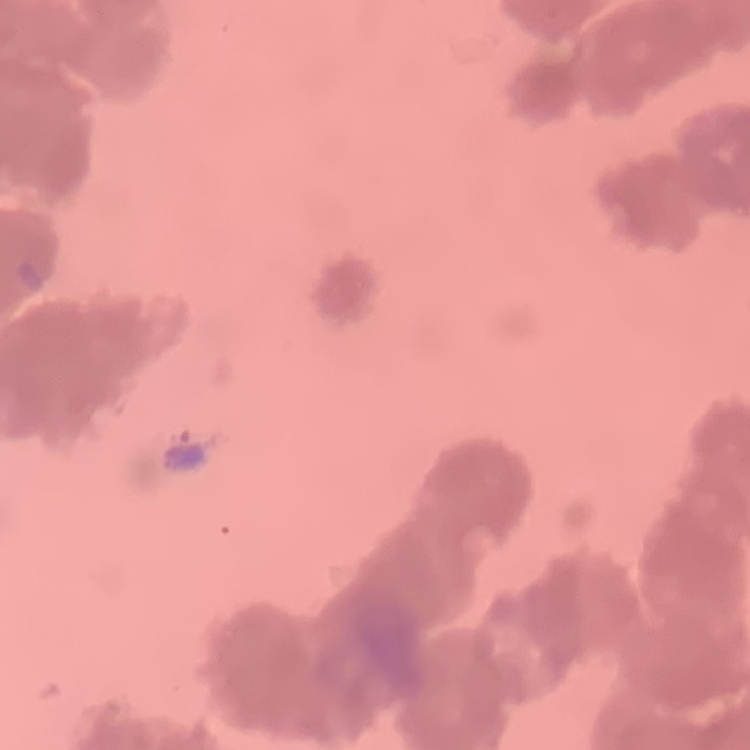 The erythrocytes exhibit rouleaux formation. Thin peripheral smear. Square crop of a larger photomicrograph. Stained with either Field's or Giemsa.